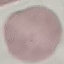

Result: no malaria parasites detected. Acquired by smartphone through the microscope eyepiece. Thin blood smear. Giemsa-stained preparation. Automatically extracted cell patch, resized to 64 × 64 pixels.